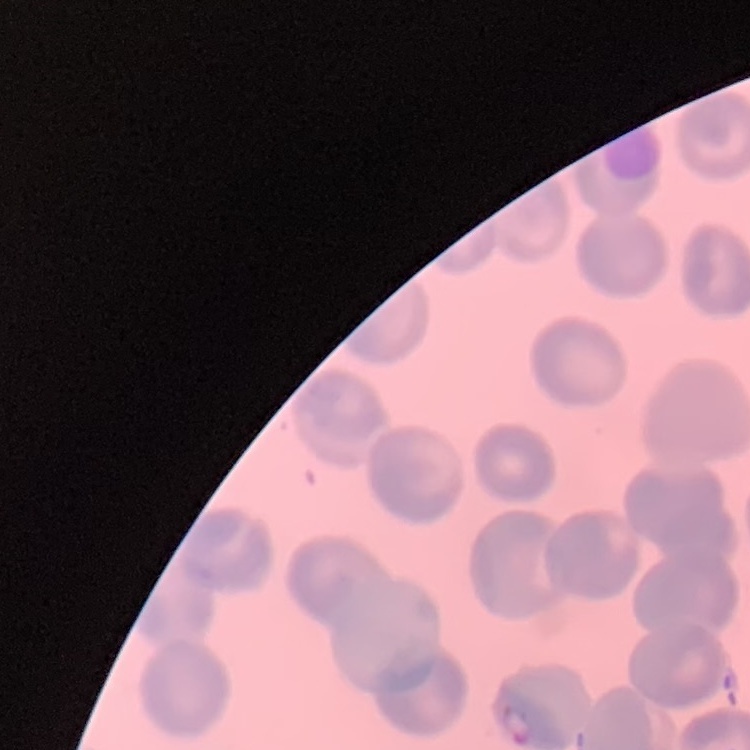

red blood cell morphology = no rouleaux formation
stain = Field's or Giemsa
image type = one tile cut from a larger photomicrograph
preparation = thin blood smear